Classify this cell by malaria status.
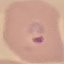
It is parasitized.

preparation: thin smear
image_type: automatically extracted cell patch, resized to 64 × 64 pixels
capture: smartphone through the microscope eyepiece
stain: Giemsa